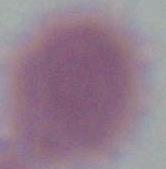
A red blood cell is seen. Photomicrograph. Captured at 1000x magnification.